Outline each blood parasite and name the species.
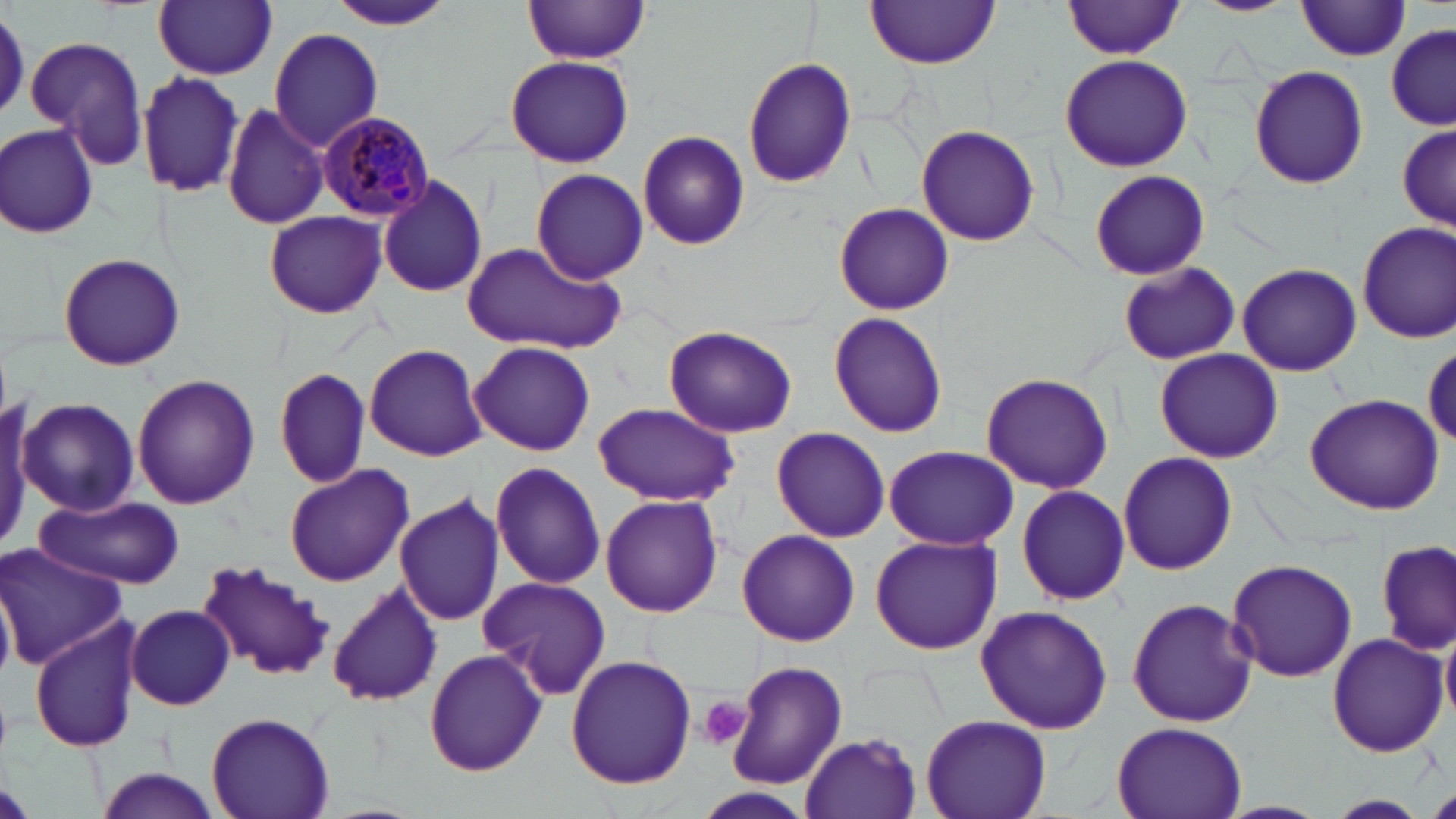
Approximate bounding boxes as (x1, y1, x2, y2) in pixels.
Plasmodium malariae-infected red blood cells: (316, 112, 435, 220).
No Plasmodium falciparum, Plasmodium ovale, Plasmodium vivax, Babesia divergens, or Trypanosoma brucei observed.

Platelet locations: (698, 695, 753, 752). Uninfected red blood cell locations: (323, 0, 457, 31), (1197, 0, 1293, 16), (153, 1, 278, 78), (867, 1, 1000, 71), (1064, 1, 1187, 58), (522, 2, 653, 63), (1296, 3, 1412, 60), (1386, 24, 1455, 128), (268, 29, 383, 152), (26, 35, 149, 171), (1059, 54, 1194, 171), (505, 55, 633, 167), (742, 57, 857, 188), (1247, 64, 1369, 190), (138, 68, 247, 199), (222, 101, 329, 231), (1394, 121, 1453, 235), (2, 122, 100, 238), (916, 125, 1040, 246), (637, 130, 750, 251), (530, 168, 649, 284), (1089, 169, 1210, 280), (377, 175, 488, 299), (835, 203, 955, 314), (265, 210, 387, 317), (1356, 220, 1456, 344), (457, 243, 624, 353), (58, 252, 186, 370), (1116, 261, 1241, 366), (1237, 263, 1361, 377), (829, 313, 948, 439), (662, 325, 799, 439), (470, 341, 595, 456), (365, 343, 487, 460), (1424, 344, 1456, 444), (1154, 348, 1282, 464), (275, 368, 370, 488), (980, 372, 1114, 494), (131, 373, 260, 510), (1304, 392, 1444, 514), (0, 396, 47, 551), (18, 397, 140, 516), (592, 403, 739, 508), (770, 428, 890, 542), (883, 444, 1019, 551), (1117, 451, 1238, 576), (488, 462, 607, 589), (284, 464, 414, 587), (1015, 485, 1131, 607), (394, 491, 505, 626), (36, 494, 186, 588), (601, 494, 723, 617), (735, 529, 859, 646), (870, 533, 1003, 654), (1378, 541, 1454, 656), (0, 545, 125, 669), (1226, 558, 1357, 683), (195, 560, 337, 681), (477, 577, 609, 700), (0, 579, 15, 686), (328, 583, 441, 707), (1128, 597, 1256, 727), (975, 604, 1113, 734), (127, 605, 234, 709), (28, 617, 144, 753), (1441, 627, 1456, 724), (1326, 632, 1449, 758), (425, 648, 548, 777), (565, 654, 696, 791), (725, 661, 847, 790), (206, 711, 333, 819), (920, 714, 1051, 819), (1111, 720, 1247, 819), (802, 732, 922, 818), (94, 765, 222, 819), (1425, 790, 1456, 819), (1320, 794, 1435, 818). Slide-level diagnosis: Plasmodium malariae. Image is 1456×819 pixels. May-Grünwald-Giemsa stain. 1000x magnification. Thin blood smear. One field of a larger specimen. Optical microscopy.